Comment on the morphology of the red blood cells.
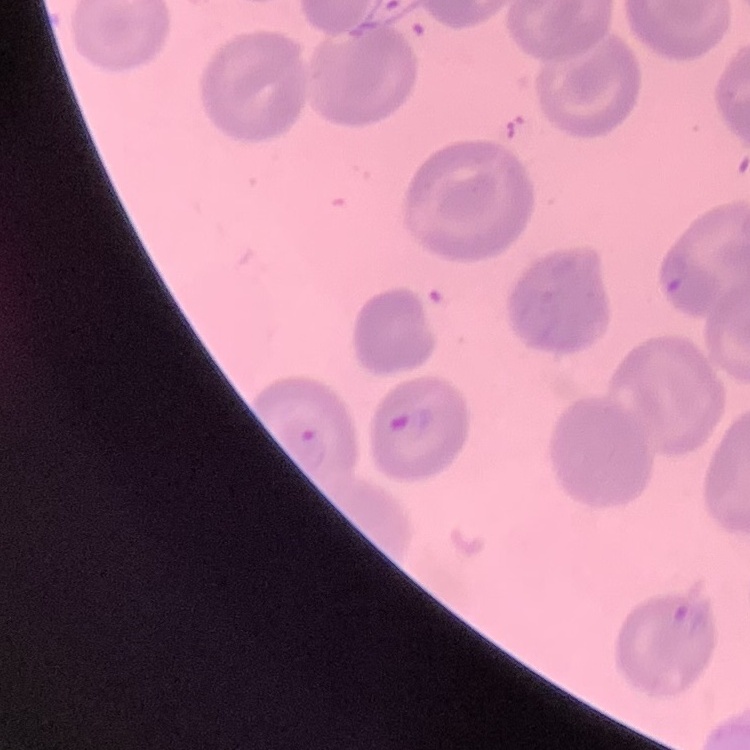
They show no rouleaux formation.

Stained with either Field's or Giemsa. Thin blood film. Square crop of a larger photomicrograph.